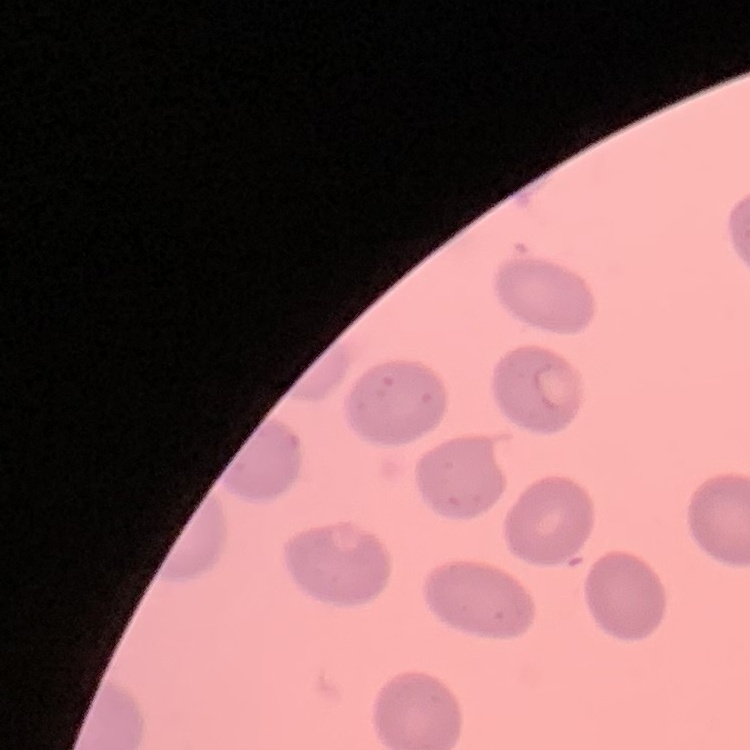
{
  "red_blood_cell_morphology": "no rouleaux formation",
  "preparation": "thin blood smear",
  "stain": "Field's or Giemsa",
  "image_type": "one tile cut from a larger photomicrograph"
}